Give the extent of all Trypanosoma brucei.
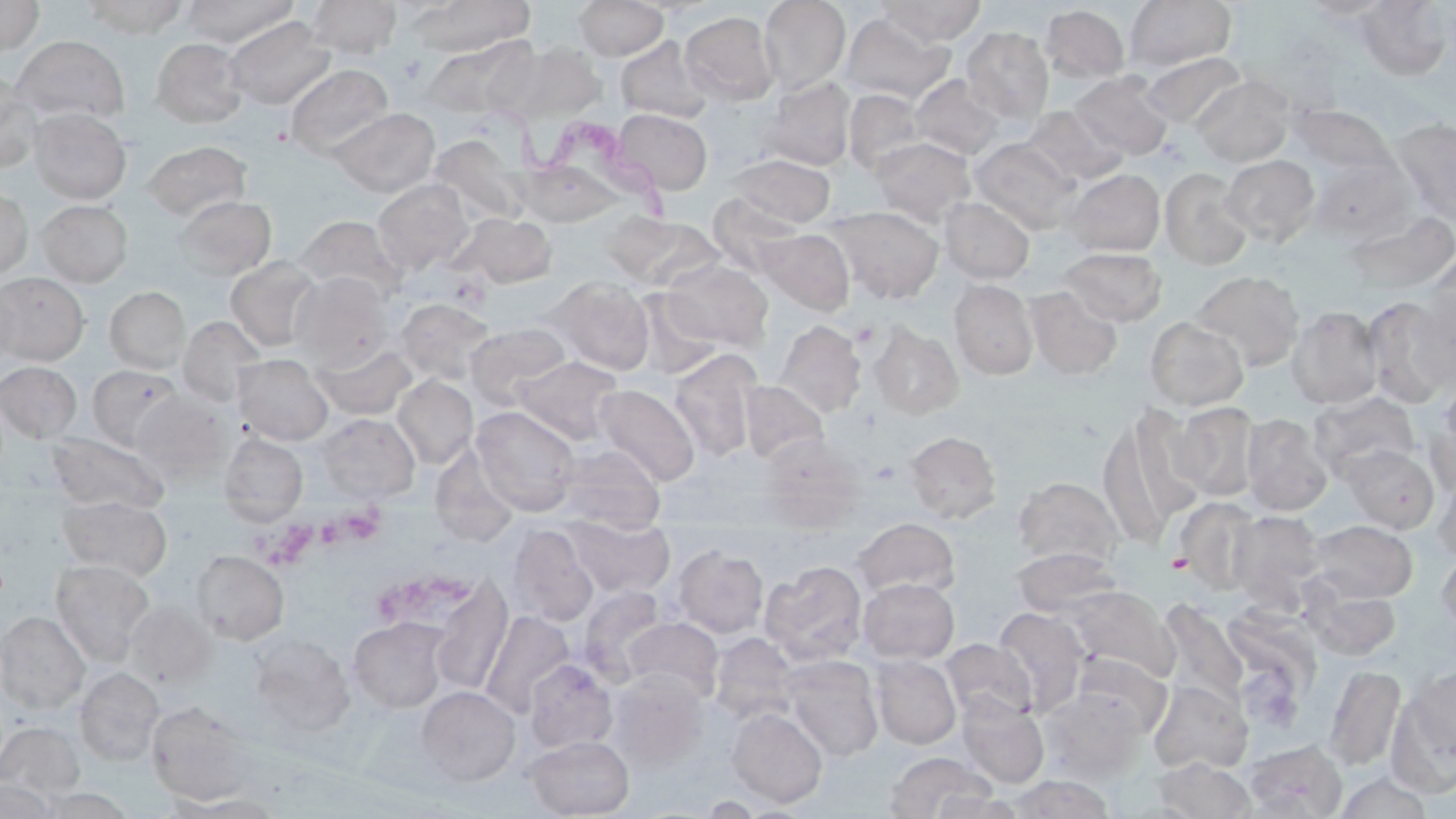

Approximate bounding boxes as (x1,y1)-(x2,y2) corner pairs in pixels.
Trypanosoma brucei: (489,98)-(678,225).

Platelet locations: (852,321)-(879,348), (870,460)-(901,484), (315,505)-(386,554), (256,515)-(319,570), (1167,552)-(1192,574), (430,570)-(471,607), (379,576)-(445,620). Uninfected red blood cell locations: (0,0)-(43,56), (82,0)-(189,39), (181,0)-(298,47), (307,0)-(401,58), (411,0)-(534,56), (758,0)-(850,95), (877,0)-(986,46), (1297,0)-(1398,21), (574,1)-(668,60), (1124,1)-(1236,72), (1354,3)-(1454,78), (1040,4)-(1130,84), (680,11)-(779,106), (838,12)-(954,105), (224,16)-(335,110), (961,26)-(1054,123), (11,35)-(130,124), (422,36)-(532,120), (616,36)-(711,123), (151,37)-(248,128), (514,43)-(606,121), (1141,52)-(1246,128), (285,64)-(393,158), (1070,71)-(1172,160), (0,73)-(43,174), (909,74)-(1007,161), (1191,74)-(1295,167), (759,76)-(856,171), (843,89)-(927,177), (1287,102)-(1395,178), (1022,105)-(1127,185), (330,107)-(439,196), (29,108)-(131,204), (613,109)-(713,195), (1389,118)-(1456,227), (869,136)-(976,226), (427,138)-(530,227), (970,138)-(1079,231), (142,141)-(252,222), (729,154)-(836,228), (1220,154)-(1320,247), (518,160)-(621,226), (1160,167)-(1254,270), (1064,169)-(1165,256), (372,179)-(473,274), (0,188)-(32,280), (708,193)-(801,276), (174,195)-(276,280), (940,197)-(1035,284), (37,199)-(133,287), (828,205)-(944,303), (1343,208)-(1455,295), (450,212)-(556,288), (606,213)-(723,294), (294,214)-(406,302), (756,228)-(855,316), (1059,247)-(1168,326), (1423,251)-(1455,351), (225,256)-(324,353), (661,258)-(773,352), (1190,270)-(1305,371), (290,272)-(393,370), (0,273)-(89,365), (548,277)-(655,375), (0,279)-(21,369), (949,279)-(1039,380), (1025,286)-(1123,379), (106,287)-(191,374), (631,290)-(726,380), (1410,292)-(1456,397), (1361,296)-(1453,407), (395,298)-(496,385), (1287,305)-(1383,409), (178,316)-(265,407), (1144,316)-(1249,411), (773,320)-(867,419), (466,323)-(571,406), (869,323)-(963,419), (313,341)-(417,420), (668,348)-(762,461), (233,354)-(333,444), (513,356)-(622,444), (0,361)-(82,443), (88,364)-(185,452), (393,375)-(478,468), (741,380)-(828,464), (593,384)-(699,487), (1424,388)-(1456,495), (132,391)-(233,483), (1309,392)-(1421,483), (1170,402)-(1262,501), (1098,403)-(1204,541), (472,406)-(581,515), (316,413)-(420,503), (1241,413)-(1333,516), (904,430)-(1001,523), (46,432)-(169,514), (219,432)-(308,525), (757,435)-(865,530), (554,444)-(665,533), (1342,444)-(1439,534), (1431,470)-(1456,563), (1013,476)-(1123,569), (58,495)-(172,580), (1174,497)-(1263,594), (1227,510)-(1325,603), (568,515)-(674,597), (852,517)-(960,600), (1308,519)-(1418,603), (509,524)-(598,627), (672,545)-(769,638), (1436,546)-(1456,640), (1011,548)-(1122,619), (191,550)-(289,644), (51,559)-(155,666), (760,560)-(869,666), (429,577)-(513,695), (858,578)-(959,663), (578,585)-(671,685), (1064,586)-(1177,683), (1307,587)-(1401,660), (1156,600)-(1249,711), (126,602)-(215,688), (992,606)-(1087,715), (479,611)-(574,718), (0,612)-(90,714), (1216,613)-(1322,734), (348,616)-(451,714), (623,617)-(724,703), (709,633)-(801,726), (249,634)-(355,736), (941,638)-(1036,724), (1071,653)-(1171,736), (871,654)-(961,749), (780,655)-(884,761), (524,659)-(618,753), (1325,665)-(1405,771), (1403,665)-(1456,771), (75,667)-(164,766), (608,671)-(709,771), (1148,680)-(1253,773), (417,686)-(521,785), (1040,686)-(1146,781), (956,694)-(1050,788), (146,702)-(257,805), (727,707)-(827,808), (0,722)-(85,797), (525,735)-(635,818), (1242,740)-(1347,818), (883,751)-(995,818), (1153,759)-(1257,817), (1333,771)-(1434,818), (1009,774)-(1115,818), (0,778)-(61,818), (931,791)-(1024,818), (166,793)-(290,817), (695,796)-(766,817). Slide-level diagnosis: Trypanosoma brucei. 1000x magnification. Light microscopy. May-Grünwald-Giemsa stain. One field of a larger specimen. Image is 1456×819 pixels. Thin blood film.